Describe the morphology of the red blood cells.
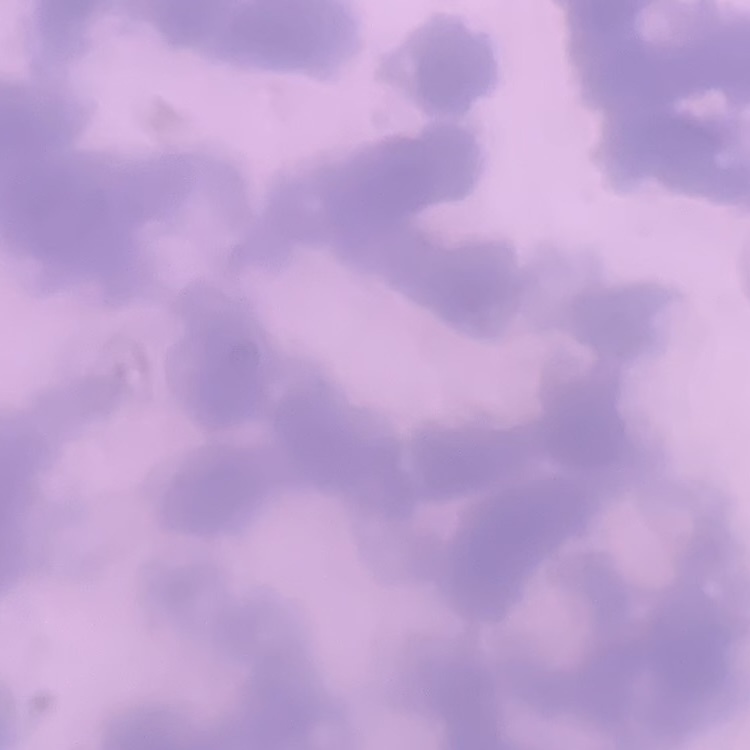

They show rouleaux formation.

Field's or Giemsa stain. Square crop of a larger photomicrograph. Thin peripheral smear.